Assess this cell for malaria.
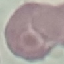
Uninfected.

{
  "capture": "smartphone camera at the microscope eyepiece",
  "stain": "Giemsa",
  "image_type": "automatically extracted cell patch, resized to 64 × 64 pixels",
  "preparation": "thin blood smear"
}